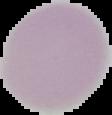 Result: negative for Plasmodium parasites. From a thin blood smear. The area outside the segmented cell region is set to black. Image is 112×115 pixels.